Locate cells.
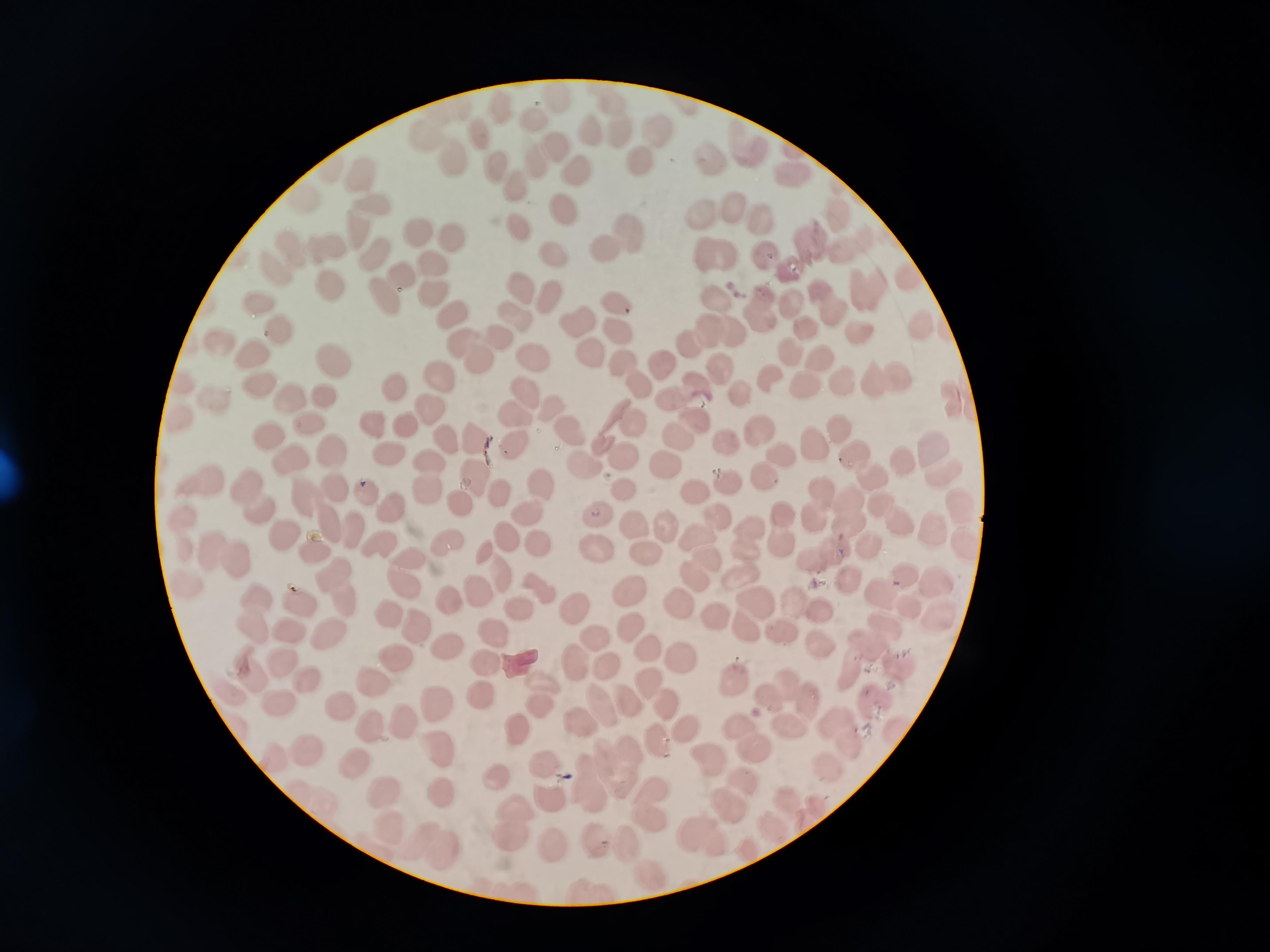

Approximate centers as (x, y) in pixels.
Cells: (619, 121), (590, 132), (658, 132), (479, 135), (754, 149), (548, 153), (642, 160), (709, 160), (460, 164), (496, 167), (581, 171), (792, 174), (365, 179), (518, 185), (735, 206), (378, 207), (565, 211), (703, 214), (763, 220), (517, 227), (418, 229), (360, 231), (616, 236), (452, 238), (815, 242), (325, 244), (295, 250), (555, 252), (716, 252), (375, 254), (767, 257), (436, 263), (788, 267), (277, 268), (329, 286), (523, 287), (394, 288), (867, 290), (438, 295), (551, 295), (619, 301), (828, 301), (715, 302), (261, 304), (796, 304), (763, 309), (451, 314), (518, 315), (581, 322), (919, 327), (280, 328), (810, 329), (621, 332), (859, 332), (711, 337), (224, 341), (478, 349), (793, 351), (256, 354), (532, 355), (594, 355), (335, 359), (661, 361), (823, 361), (627, 370), (719, 370), (442, 377), (771, 380), (843, 380), (889, 382), (806, 383), (640, 385), (263, 386), (394, 388), (526, 391), (681, 392), (325, 396), (216, 400), (293, 400), (552, 407), (435, 410), (517, 417), (699, 421), (309, 422), (373, 424), (630, 425), (408, 427), (838, 428), (574, 430), (761, 432), (678, 436), (266, 437), (451, 438), (479, 439), (517, 441), (725, 443), (814, 445), (934, 446), (332, 450), (387, 453), (783, 453), (623, 454), (855, 456), (293, 459), (903, 460), (666, 464), (587, 466), (428, 475), (764, 477), (475, 478), (876, 478), (198, 480), (729, 485), (544, 487), (625, 489), (368, 493), (498, 495), (693, 495), (255, 500), (465, 505), (394, 506), (819, 506), (323, 508), (964, 509), (849, 511), (598, 513), (528, 517), (718, 517), (891, 517), (637, 523), (666, 527), (786, 527), (350, 532), (938, 533), (283, 537), (507, 537), (745, 537), (537, 544), (448, 545), (868, 546), (377, 547), (486, 553), (600, 553), (309, 554), (647, 554), (826, 554), (225, 555), (700, 555), (409, 560), (501, 576), (746, 577), (849, 580), (405, 582), (940, 582), (342, 587), (545, 589), (480, 593), (885, 593), (634, 594), (454, 600), (679, 601), (759, 601), (519, 602), (302, 604), (803, 606), (578, 608), (258, 611), (389, 615), (717, 616), (418, 627), (291, 630), (631, 630), (751, 630), (493, 631), (329, 632), (878, 633), (783, 636), (597, 640), (447, 645), (649, 647), (682, 657), (396, 659), (574, 662), (280, 664), (487, 665), (898, 665), (608, 669), (851, 672), (307, 678), (374, 680), (646, 680), (736, 683), (793, 691), (481, 693), (542, 694), (445, 701), (280, 702), (629, 702), (667, 702), (875, 703), (339, 705), (604, 708), (408, 724), (583, 724), (789, 725), (689, 727), (371, 730), (521, 731), (844, 731), (658, 737), (752, 737), (440, 746), (296, 750), (548, 762), (710, 762), (355, 763), (621, 766), (830, 770), (498, 775), (743, 780), (593, 783), (383, 790), (443, 790), (552, 797), (787, 801), (650, 802), (735, 804), (512, 824), (393, 826), (773, 830), (706, 833), (614, 842), (552, 844), (439, 847), (652, 875).

capture: smartphone through the microscope eyepiece
preparation: thin blood smear
stain: Giemsa
image_size: 1270×952 pixels
field_of_view: single